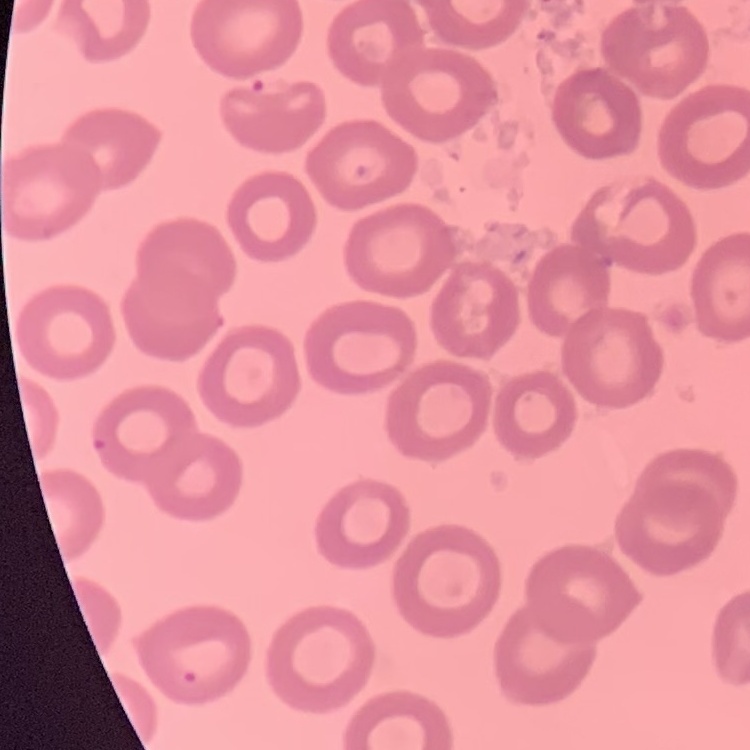

red blood cell morphology = no rouleaux formation
preparation = thin peripheral smear
stain = Field's or Giemsa
image type = one tile cut from a larger photomicrograph